Report the malaria status of this cell.
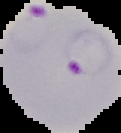

It is parasitized.

The area outside the segmented cell region is set to black. Image is 121×133 pixels. From a thin blood film.